Outline each blood parasite and name the species.
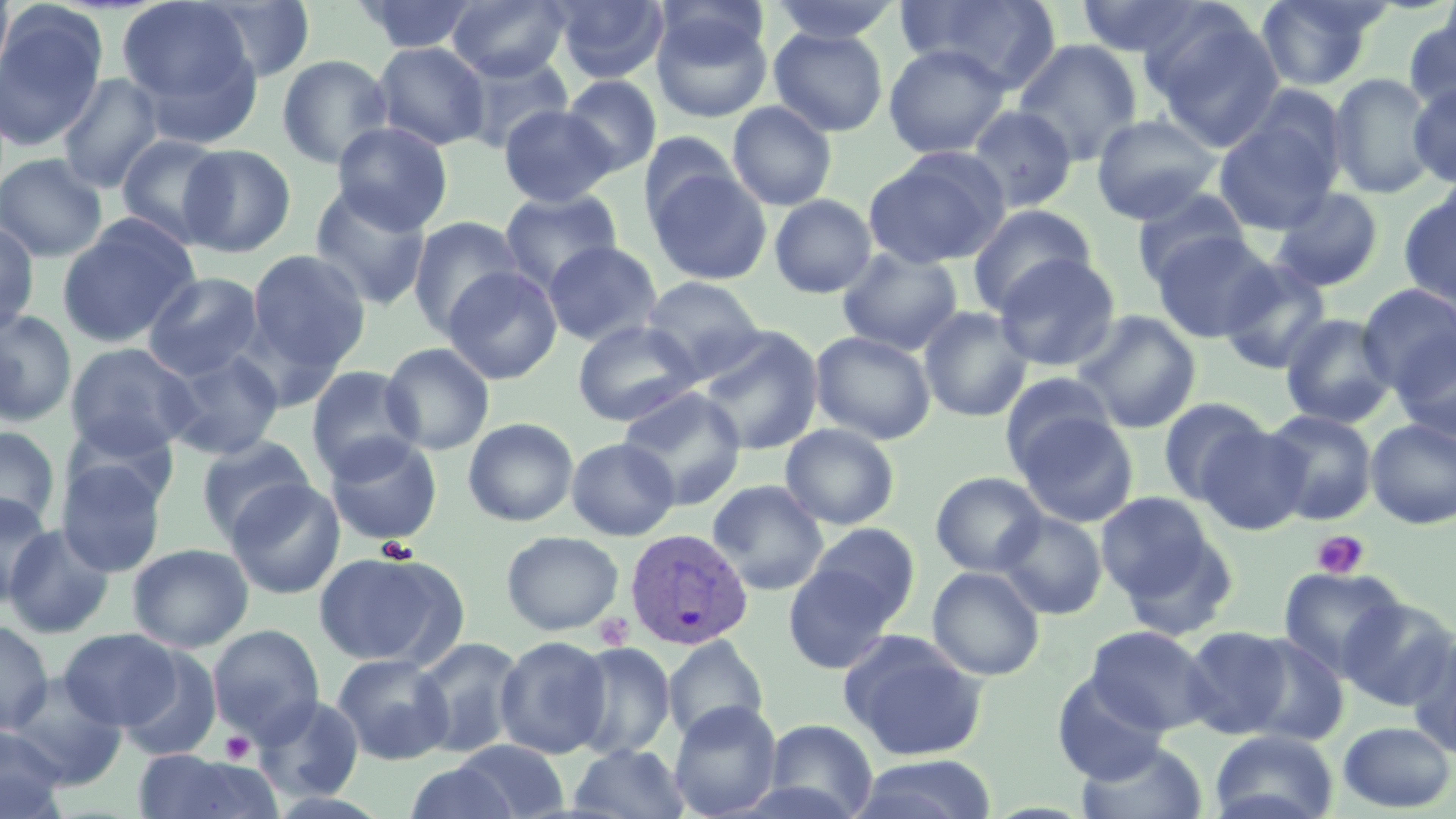

Approximate bounding boxes as [x1, y1, x2, y2] in pixels.
Plasmodium vivax-infected red blood cells: [624, 526, 754, 650].
No Plasmodium falciparum, Plasmodium ovale, Plasmodium malariae, Babesia divergens, or Trypanosoma brucei observed.

Uninfected red blood cell locations: [0, 0, 16, 92], [116, 0, 258, 125], [355, 0, 481, 55], [447, 0, 570, 82], [552, 0, 668, 84], [768, 0, 903, 44], [896, 0, 1063, 92], [1076, 0, 1213, 60], [1255, 0, 1383, 90], [1437, 0, 1456, 66], [196, 1, 317, 84], [0, 6, 108, 153], [651, 12, 772, 124], [1147, 13, 1285, 150], [1403, 16, 1456, 114], [768, 27, 889, 136], [1012, 39, 1142, 165], [371, 42, 491, 151], [882, 43, 1012, 159], [458, 51, 574, 154], [276, 54, 393, 170], [56, 73, 165, 193], [1328, 73, 1437, 198], [561, 75, 662, 178], [1408, 83, 1456, 188], [727, 100, 837, 211], [498, 104, 617, 207], [966, 104, 1078, 213], [1090, 113, 1222, 224], [1213, 115, 1340, 235], [332, 121, 454, 234], [640, 132, 741, 228], [116, 133, 229, 249], [179, 144, 296, 257], [862, 148, 1009, 269], [0, 153, 108, 262], [648, 167, 772, 286], [309, 184, 432, 310], [1131, 187, 1250, 288], [1270, 187, 1384, 292], [499, 190, 622, 294], [1398, 192, 1456, 309], [769, 194, 877, 298], [967, 204, 1096, 315], [57, 215, 199, 349], [407, 216, 525, 336], [0, 222, 39, 335], [1152, 231, 1277, 342], [543, 240, 662, 346], [837, 248, 963, 355], [246, 250, 371, 374], [994, 253, 1120, 371], [1217, 258, 1333, 374], [442, 266, 563, 384], [142, 272, 264, 380], [641, 275, 766, 379], [1357, 283, 1456, 393], [918, 305, 1033, 422], [0, 309, 77, 427], [1074, 311, 1201, 433], [1280, 313, 1396, 427], [572, 320, 702, 425], [695, 326, 823, 456], [810, 330, 937, 445], [1393, 332, 1456, 444], [380, 342, 495, 455], [64, 343, 200, 458], [159, 348, 285, 460], [305, 365, 422, 478], [1000, 371, 1118, 473], [619, 388, 747, 508], [1157, 397, 1270, 504], [1263, 409, 1377, 525], [1013, 411, 1138, 527], [463, 417, 579, 526], [1366, 420, 1456, 529], [63, 421, 180, 512], [780, 423, 900, 530], [1199, 424, 1311, 535], [0, 426, 60, 530], [324, 433, 443, 545], [197, 434, 316, 541], [566, 436, 680, 540], [56, 459, 168, 576], [930, 471, 1047, 576], [226, 478, 345, 599], [707, 480, 828, 595], [1096, 491, 1218, 603], [1, 493, 55, 606], [994, 511, 1107, 619], [1, 523, 116, 638], [804, 523, 921, 628], [501, 530, 624, 636], [127, 543, 253, 653], [312, 551, 461, 667], [782, 559, 902, 673], [926, 566, 1046, 681], [1278, 567, 1407, 678], [1338, 598, 1456, 710], [0, 621, 53, 734], [207, 624, 325, 744], [1085, 625, 1215, 735], [1181, 626, 1294, 738], [58, 628, 182, 730], [838, 630, 988, 761], [1407, 631, 1456, 759], [495, 635, 612, 759], [1239, 635, 1348, 746], [409, 636, 528, 758], [662, 637, 770, 742], [570, 642, 676, 760], [116, 646, 222, 760], [332, 653, 454, 765], [5, 673, 128, 789], [1052, 674, 1169, 784], [252, 694, 366, 803], [669, 700, 782, 818], [763, 718, 879, 818], [1337, 720, 1455, 813], [0, 725, 68, 818], [1209, 730, 1338, 819], [451, 739, 571, 818], [1076, 740, 1208, 819], [567, 743, 692, 819], [131, 751, 283, 818], [850, 754, 998, 819], [403, 762, 521, 819]. Platelet locations: [1311, 530, 1370, 579], [376, 537, 418, 564], [594, 613, 634, 650], [220, 731, 255, 764]. Slide-level diagnosis: Plasmodium vivax. One field of a larger specimen. Thin blood film. May-Grünwald-Giemsa stain. Light microscopy. Captured at 1000x magnification. Image is 1456×819 pixels.